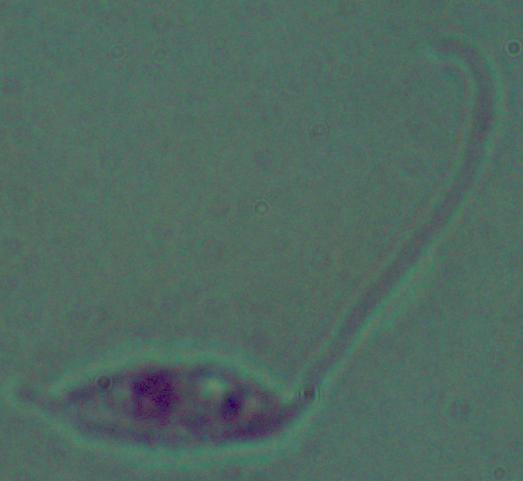 Micrograph. A Leishmania parasite is shown. Captured at 1000x magnification.